State which parasite is depicted.
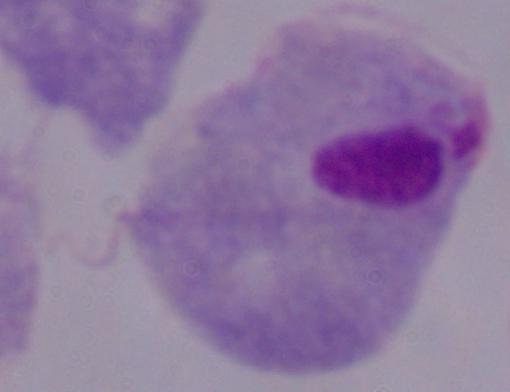
This is a trichomonad.

Captured at 1000x magnification. Micrograph.